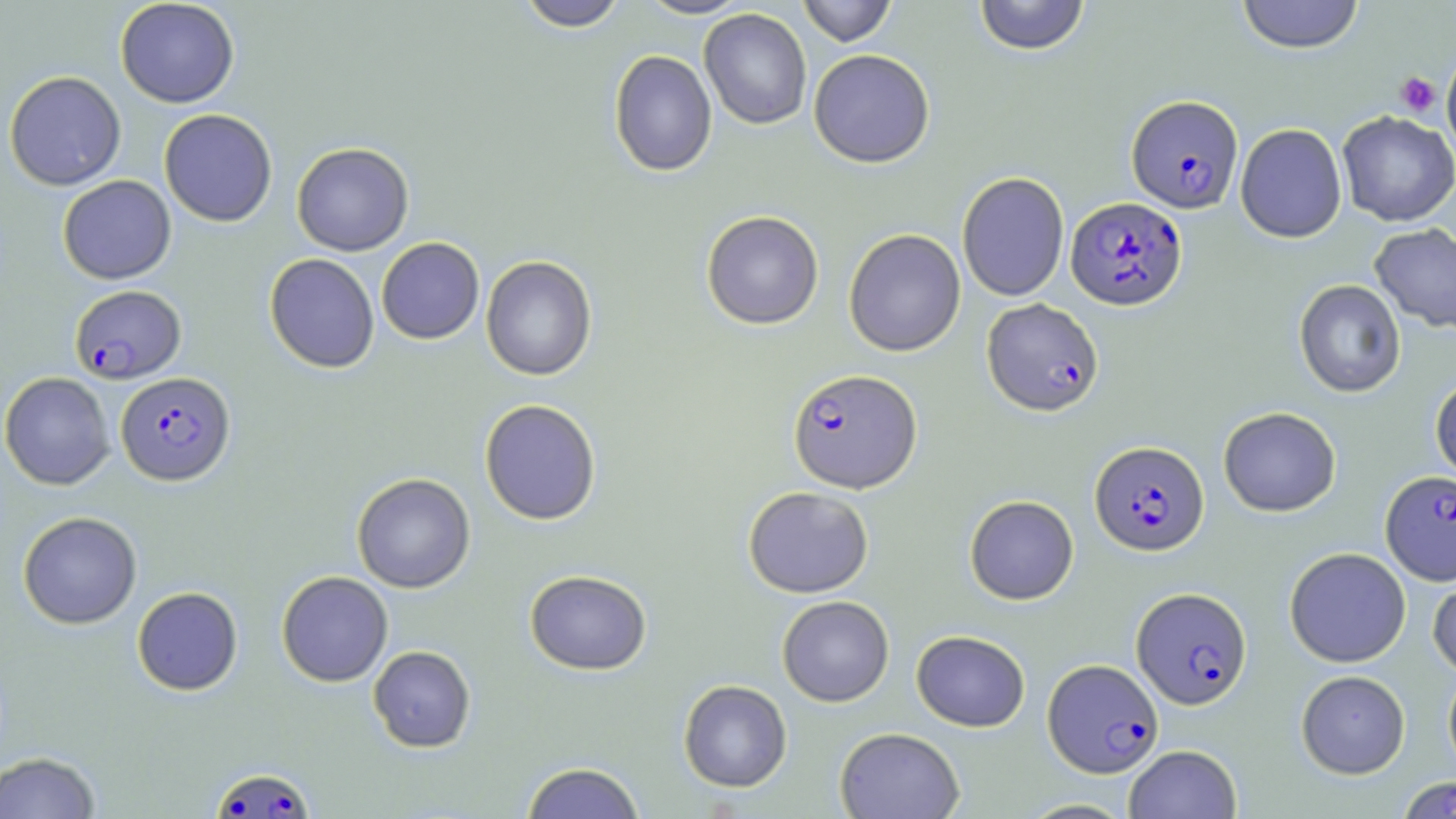

Summary:
  - Coordinate format: approximate bounding boxes as [x1, y1, x2, y2] in pixels
  - Uninfected red blood cell locations: [115, 0, 239, 108], [515, 0, 629, 31], [637, 0, 753, 19], [798, 0, 897, 47], [973, 0, 1091, 56], [1235, 0, 1365, 54], [699, 8, 812, 130], [608, 49, 717, 177], [808, 49, 935, 168], [1441, 52, 1456, 159], [4, 70, 126, 191], [159, 109, 277, 227], [1337, 111, 1456, 227], [1235, 123, 1347, 242], [291, 142, 414, 256], [956, 171, 1069, 302], [57, 175, 176, 284], [701, 210, 824, 329], [1369, 223, 1456, 334], [843, 228, 966, 357], [376, 237, 484, 344], [265, 253, 380, 373], [481, 255, 597, 381], [1294, 279, 1406, 397], [0, 372, 116, 490], [1430, 373, 1456, 487], [479, 398, 602, 525], [1218, 407, 1341, 517], [352, 473, 475, 593], [743, 486, 874, 598], [965, 495, 1079, 605], [18, 511, 142, 629], [1284, 547, 1411, 667], [1428, 567, 1456, 678], [525, 569, 652, 675], [276, 571, 393, 687], [132, 586, 243, 696], [777, 595, 894, 706], [911, 630, 1030, 731], [368, 645, 476, 752], [1443, 665, 1456, 779], [1296, 670, 1410, 779], [678, 679, 793, 792], [835, 727, 965, 818], [1123, 744, 1242, 818], [0, 752, 101, 818], [521, 762, 646, 819]
  - Platelet locations: [1395, 72, 1442, 116]
  - Plasmodium falciparum-infected red blood cell locations: [1126, 94, 1243, 213], [1066, 196, 1187, 311], [70, 285, 186, 384], [982, 298, 1104, 416], [787, 368, 922, 493], [116, 371, 235, 486], [1089, 440, 1210, 556], [1380, 470, 1456, 586], [1132, 587, 1252, 709], [1043, 658, 1163, 778], [210, 767, 315, 818], [1397, 776, 1456, 817]
  - Slide-level diagnosis: Plasmodium falciparum
  - Stain: May-Grünwald-Giemsa
  - Magnification: 1000x
  - Modality: optical microscopy
  - Preparation: thin blood film
  - Image size: 1456×819 pixels
  - Field of view: single